Assess the morphology of the erythrocytes.
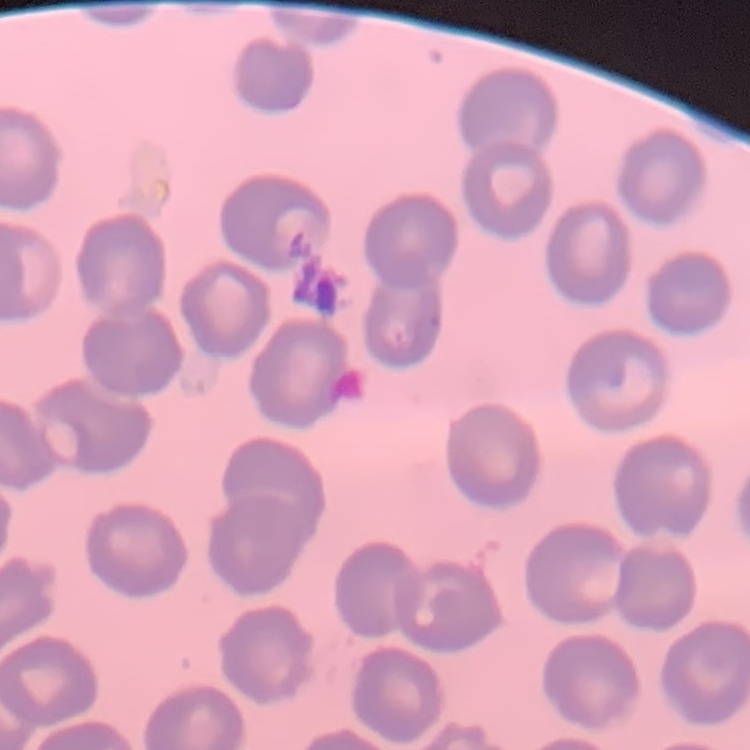
No rouleaux formation.

Summary:
  - Stain: Field's or Giemsa
  - Image type: one tile cut from a larger photomicrograph
  - Preparation: thin peripheral smear